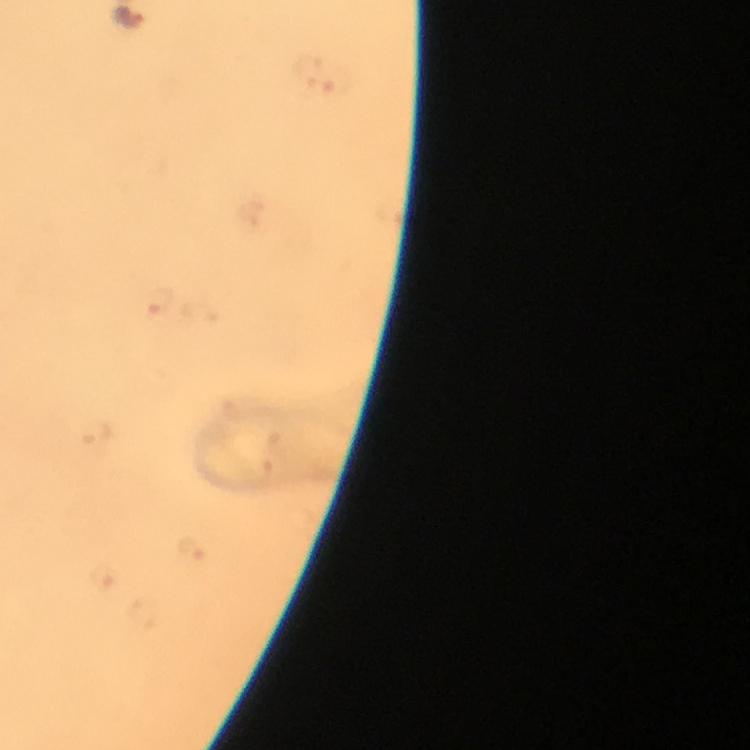 Approximate object centers, in pixels from the top-left corner. Malaria parasite locations: (x=131, y=22), (x=158, y=303). Immersion oil applied. Photographed with a smartphone mounted on the microscope. A crop from one field of view. Image is 750×750 pixels. Giemsa stain. 100x magnification. From a malaria diagnostic workup. Thick blood smear.